State which cell type is depicted.
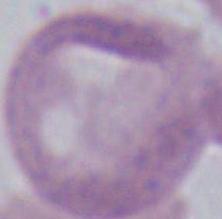

This is an erythrocyte.

Photomicrograph. Captured at 1000x magnification.